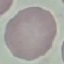 Malaria status: uninfected. Acquired by smartphone through the microscope eyepiece. Cell patch, automatically extracted from a larger field of view and resized to 64 × 64 pixels. Giemsa stain. Thin blood film.